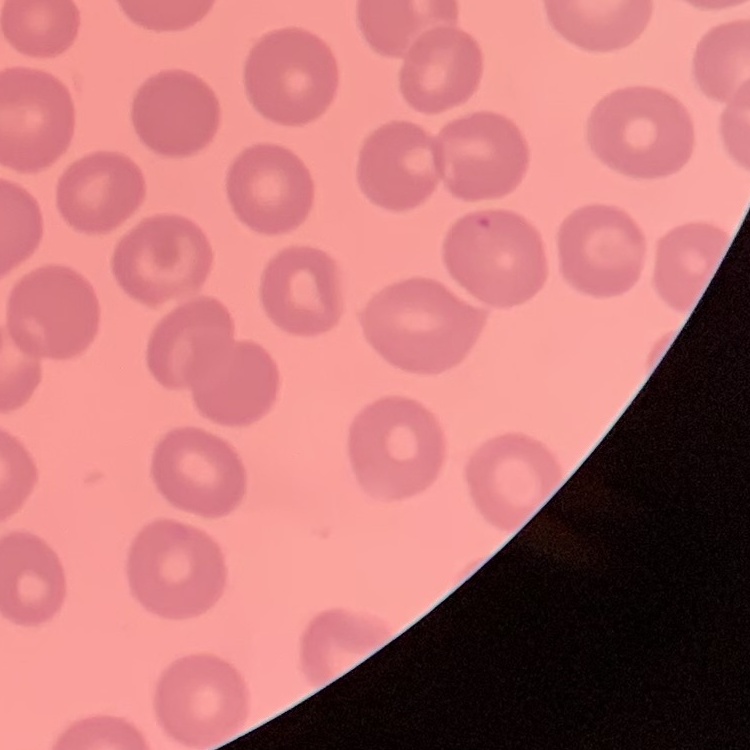

Summary:
  - Red blood cell morphology: no rouleaux formation
  - Preparation: thin blood film
  - Image type: square crop of a larger photomicrograph
  - Stain: Field's or Giemsa